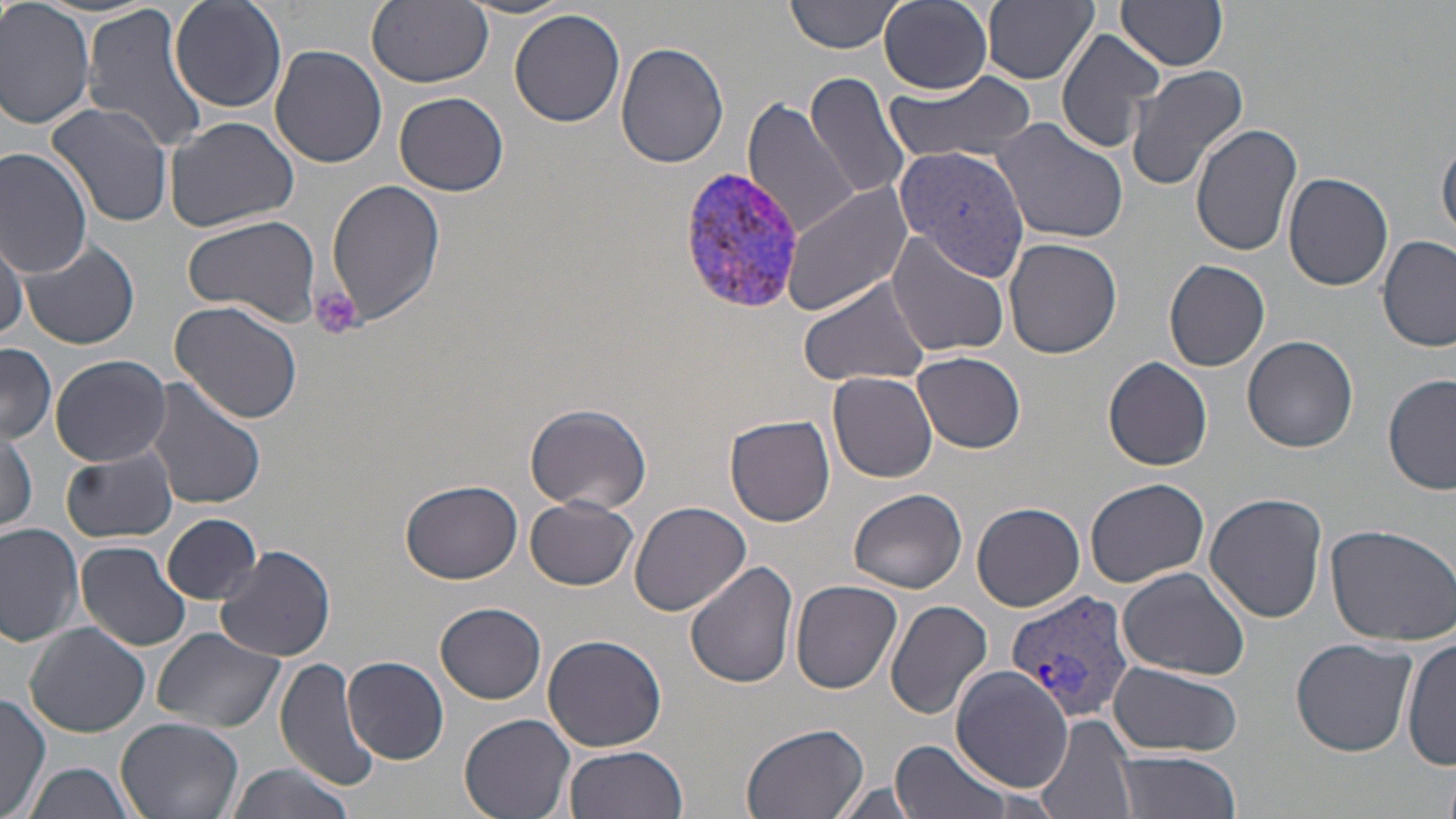
Approximate bounding boxes as named x1/y1/x2/y2 corners in pixels. Uninfected red blood cell locations: (x1=0, y1=0, x2=98, y2=132), (x1=788, y1=0, x2=905, y2=55), (x1=880, y1=0, x2=993, y2=93), (x1=169, y1=1, x2=286, y2=112), (x1=365, y1=1, x2=494, y2=88), (x1=981, y1=1, x2=1099, y2=85), (x1=1114, y1=1, x2=1231, y2=71), (x1=459, y1=2, x2=580, y2=21), (x1=82, y1=3, x2=210, y2=152), (x1=510, y1=8, x2=626, y2=128), (x1=1055, y1=26, x2=1166, y2=152), (x1=615, y1=41, x2=731, y2=169), (x1=269, y1=43, x2=388, y2=169), (x1=1126, y1=64, x2=1250, y2=190), (x1=803, y1=71, x2=911, y2=203), (x1=883, y1=73, x2=1036, y2=166), (x1=393, y1=90, x2=509, y2=198), (x1=744, y1=98, x2=860, y2=241), (x1=45, y1=101, x2=175, y2=230), (x1=163, y1=116, x2=299, y2=233), (x1=993, y1=116, x2=1132, y2=244), (x1=1190, y1=124, x2=1303, y2=257), (x1=1437, y1=134, x2=1456, y2=242), (x1=898, y1=137, x2=1034, y2=283), (x1=0, y1=147, x2=96, y2=278), (x1=1284, y1=172, x2=1393, y2=292), (x1=327, y1=179, x2=445, y2=329), (x1=781, y1=183, x2=913, y2=317), (x1=182, y1=215, x2=322, y2=324), (x1=0, y1=229, x2=27, y2=341), (x1=885, y1=232, x2=1010, y2=357), (x1=1377, y1=234, x2=1455, y2=352), (x1=1003, y1=238, x2=1123, y2=358), (x1=17, y1=241, x2=140, y2=349), (x1=1164, y1=258, x2=1270, y2=371), (x1=796, y1=274, x2=933, y2=389), (x1=169, y1=299, x2=304, y2=426), (x1=1244, y1=335, x2=1360, y2=453), (x1=0, y1=343, x2=58, y2=444), (x1=912, y1=351, x2=1026, y2=452), (x1=46, y1=355, x2=175, y2=467), (x1=1103, y1=356, x2=1213, y2=470), (x1=828, y1=371, x2=938, y2=484), (x1=1383, y1=374, x2=1455, y2=496), (x1=144, y1=377, x2=267, y2=512), (x1=524, y1=401, x2=652, y2=513), (x1=723, y1=414, x2=836, y2=528), (x1=0, y1=428, x2=38, y2=536), (x1=61, y1=448, x2=179, y2=544), (x1=1085, y1=476, x2=1210, y2=588), (x1=1097, y1=479, x2=1228, y2=675), (x1=402, y1=480, x2=523, y2=582), (x1=849, y1=488, x2=967, y2=595), (x1=1205, y1=491, x2=1327, y2=623), (x1=526, y1=495, x2=637, y2=591), (x1=628, y1=500, x2=751, y2=618), (x1=971, y1=501, x2=1085, y2=611), (x1=161, y1=513, x2=262, y2=604), (x1=1323, y1=520, x2=1456, y2=646), (x1=0, y1=522, x2=85, y2=646), (x1=77, y1=540, x2=192, y2=651), (x1=217, y1=545, x2=335, y2=662), (x1=684, y1=561, x2=799, y2=689), (x1=1117, y1=568, x2=1250, y2=679), (x1=790, y1=579, x2=903, y2=694), (x1=884, y1=600, x2=993, y2=721), (x1=436, y1=602, x2=547, y2=704), (x1=23, y1=621, x2=151, y2=737), (x1=151, y1=628, x2=286, y2=734), (x1=1403, y1=632, x2=1455, y2=773), (x1=542, y1=634, x2=670, y2=752), (x1=1290, y1=637, x2=1417, y2=755), (x1=276, y1=655, x2=382, y2=794), (x1=343, y1=656, x2=448, y2=764), (x1=1108, y1=662, x2=1241, y2=756), (x1=950, y1=664, x2=1073, y2=790), (x1=0, y1=694, x2=51, y2=819), (x1=458, y1=712, x2=574, y2=819), (x1=1035, y1=714, x2=1138, y2=819), (x1=116, y1=717, x2=243, y2=819), (x1=740, y1=723, x2=870, y2=819), (x1=887, y1=738, x2=1014, y2=819), (x1=561, y1=745, x2=688, y2=819), (x1=1109, y1=751, x2=1241, y2=818), (x1=22, y1=763, x2=137, y2=819), (x1=222, y1=763, x2=359, y2=819), (x1=826, y1=781, x2=930, y2=819). Plasmodium vivax-infected red blood cell locations: (x1=674, y1=168, x2=812, y2=316), (x1=1008, y1=589, x2=1136, y2=722). Platelet locations: (x1=310, y1=286, x2=364, y2=341). Slide-level diagnosis: Plasmodium vivax. 1000x magnification. Image is 1456×819 pixels. Thin blood film. Single field of view. Optical microscopy. May-Grünwald-Giemsa stain.